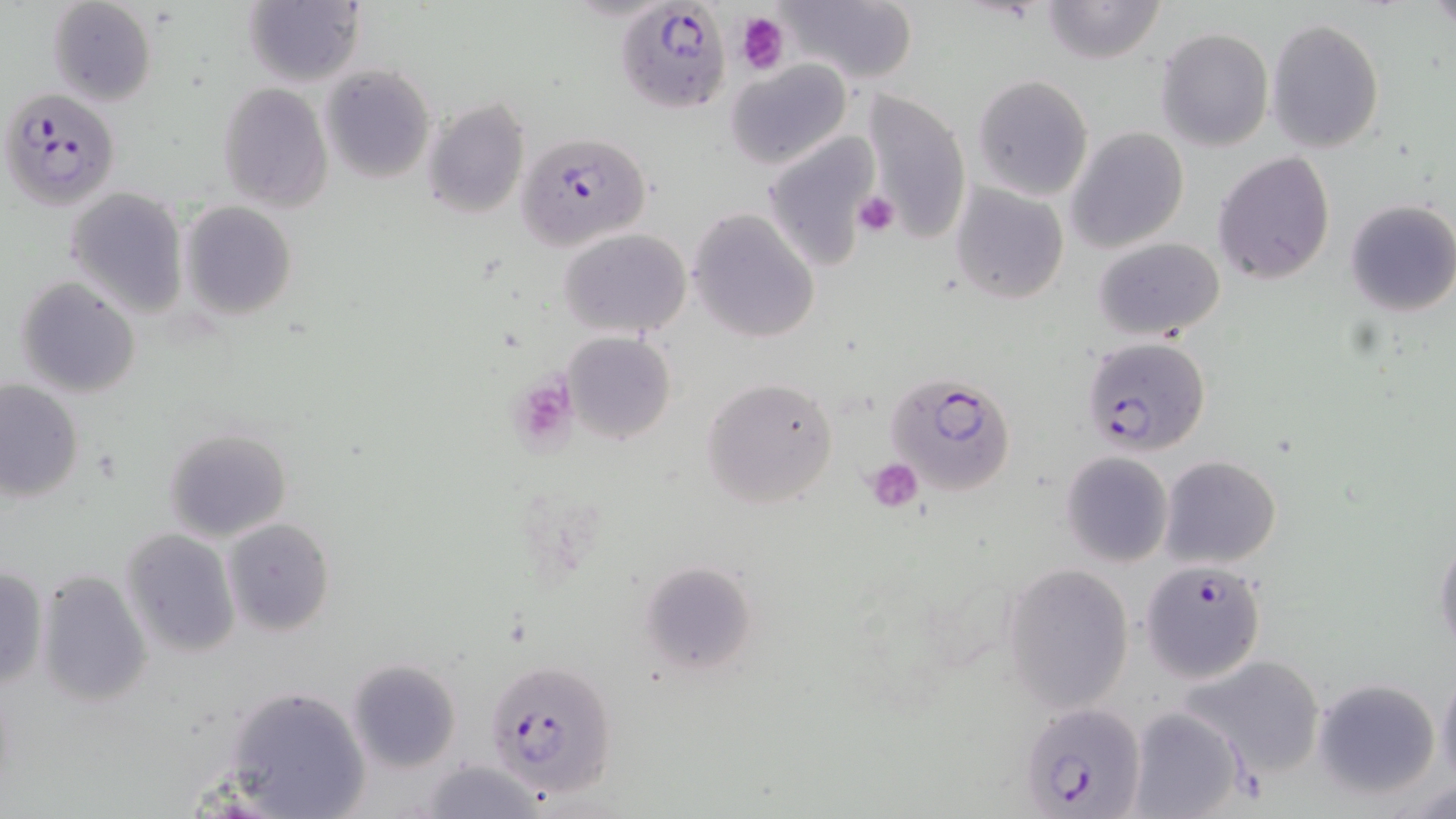

Summary:
  - Coordinate format: approximate bounding boxes as named x1/y1/x2/y2 corners in pixels
  - Uninfected red blood cell locations: (x1=47, y1=0, x2=158, y2=106), (x1=780, y1=0, x2=920, y2=86), (x1=1040, y1=0, x2=1166, y2=64), (x1=242, y1=2, x2=366, y2=87), (x1=1266, y1=17, x2=1385, y2=153), (x1=1156, y1=27, x2=1273, y2=151), (x1=726, y1=61, x2=852, y2=170), (x1=320, y1=65, x2=435, y2=185), (x1=970, y1=74, x2=1093, y2=201), (x1=216, y1=82, x2=333, y2=211), (x1=863, y1=90, x2=972, y2=234), (x1=423, y1=99, x2=532, y2=219), (x1=1066, y1=126, x2=1189, y2=253), (x1=761, y1=129, x2=882, y2=269), (x1=1213, y1=151, x2=1335, y2=286), (x1=949, y1=183, x2=1070, y2=304), (x1=65, y1=185, x2=190, y2=318), (x1=1343, y1=200, x2=1456, y2=317), (x1=179, y1=202, x2=298, y2=319), (x1=686, y1=209, x2=819, y2=343), (x1=559, y1=228, x2=692, y2=338), (x1=1092, y1=236, x2=1225, y2=342), (x1=13, y1=276, x2=142, y2=399), (x1=561, y1=331, x2=678, y2=444), (x1=701, y1=377, x2=841, y2=509), (x1=0, y1=379, x2=84, y2=502), (x1=162, y1=426, x2=292, y2=541), (x1=1060, y1=450, x2=1173, y2=567), (x1=1159, y1=456, x2=1283, y2=569), (x1=223, y1=518, x2=333, y2=636), (x1=120, y1=527, x2=243, y2=658), (x1=1434, y1=533, x2=1456, y2=657), (x1=640, y1=560, x2=759, y2=675), (x1=1002, y1=562, x2=1135, y2=713), (x1=0, y1=564, x2=49, y2=692), (x1=35, y1=570, x2=153, y2=708), (x1=1180, y1=652, x2=1328, y2=778), (x1=346, y1=659, x2=463, y2=771), (x1=1436, y1=663, x2=1456, y2=791), (x1=1311, y1=677, x2=1442, y2=798), (x1=223, y1=682, x2=371, y2=818), (x1=1129, y1=707, x2=1245, y2=819), (x1=418, y1=759, x2=552, y2=817)
  - Plasmodium falciparum-infected red blood cell locations: (x1=609, y1=2, x2=737, y2=121), (x1=2, y1=87, x2=120, y2=210), (x1=518, y1=131, x2=652, y2=250), (x1=1081, y1=336, x2=1211, y2=458), (x1=888, y1=372, x2=1018, y2=496), (x1=1139, y1=558, x2=1268, y2=685), (x1=484, y1=658, x2=619, y2=798), (x1=1020, y1=703, x2=1147, y2=817)
  - Platelet locations: (x1=736, y1=11, x2=786, y2=73), (x1=853, y1=190, x2=901, y2=238), (x1=521, y1=383, x2=578, y2=450), (x1=866, y1=457, x2=924, y2=512)
  - Slide-level diagnosis: Plasmodium falciparum
  - Field of view: single
  - Image size: 1456×819 pixels
  - Magnification: 1000x
  - Preparation: thin blood film
  - Modality: light microscopy
  - Stain: May-Grünwald-Giemsa